Name the parasite shown.
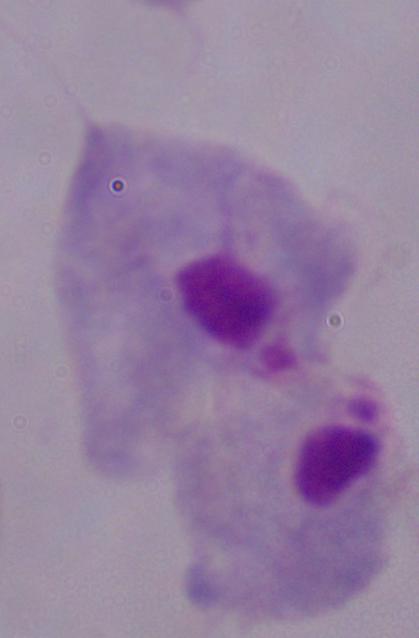

A trichomonad.

Summary:
  - Modality: photomicrograph
  - Magnification: 1000x